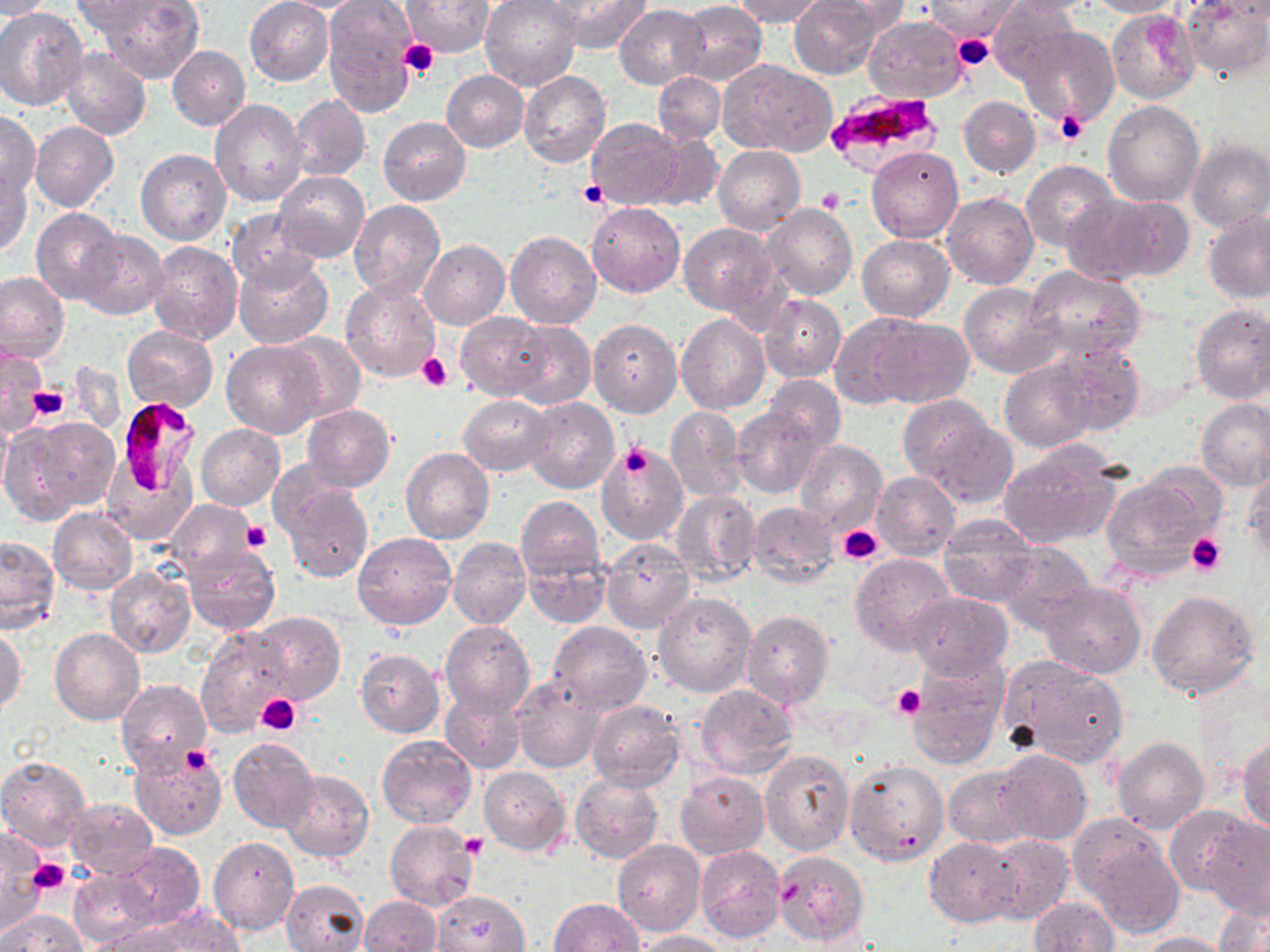
Summary:
  - Coordinate format: approximate bounding boxes as (x1, y1, x2, y2) in pixels
  - Uninfected red blood cell locations: (0, 0, 56, 19), (93, 0, 205, 84), (245, 0, 334, 85), (322, 0, 418, 118), (480, 0, 581, 92), (548, 0, 653, 52), (732, 0, 827, 26), (790, 0, 884, 79), (820, 0, 910, 39), (923, 0, 1022, 40), (987, 0, 1082, 89), (1002, 0, 1107, 15), (1087, 0, 1185, 18), (1181, 0, 1269, 81), (71, 1, 170, 37), (402, 1, 493, 57), (675, 2, 766, 84), (490, 5, 592, 165), (615, 5, 709, 89), (0, 8, 87, 111), (1107, 9, 1200, 104), (864, 15, 966, 104), (1021, 27, 1119, 128), (168, 45, 251, 132), (60, 47, 152, 140), (719, 60, 834, 156), (441, 70, 528, 152), (519, 70, 611, 168), (653, 71, 725, 144), (291, 95, 371, 181), (958, 96, 1039, 177), (210, 99, 307, 206), (1103, 99, 1204, 208), (0, 112, 40, 198), (379, 117, 471, 206), (584, 118, 682, 209), (30, 122, 119, 212), (651, 132, 724, 212), (1187, 140, 1270, 233), (713, 145, 805, 235), (867, 145, 963, 242), (136, 149, 232, 245), (1022, 160, 1120, 255), (0, 169, 32, 256), (274, 170, 369, 263), (942, 193, 1038, 290), (1063, 196, 1157, 282), (1105, 197, 1194, 281), (347, 200, 447, 302), (759, 202, 857, 300), (587, 203, 685, 297), (32, 207, 123, 304), (227, 209, 320, 291), (1203, 212, 1270, 304), (679, 223, 779, 319), (74, 231, 169, 320), (505, 231, 601, 328), (856, 235, 955, 322), (419, 239, 510, 330), (148, 241, 243, 346), (233, 255, 333, 349), (1024, 265, 1146, 363), (0, 272, 69, 365), (340, 278, 439, 380), (959, 282, 1061, 378), (759, 295, 846, 382), (1190, 304, 1270, 405), (455, 312, 553, 400), (676, 312, 770, 413), (830, 313, 932, 409), (866, 317, 974, 409), (588, 318, 682, 418), (506, 319, 595, 409), (123, 326, 217, 412), (276, 333, 366, 422), (1049, 340, 1144, 436), (221, 341, 326, 437), (0, 346, 46, 434), (1000, 359, 1098, 453), (761, 374, 846, 452), (458, 395, 552, 476), (521, 396, 620, 495), (1196, 399, 1270, 490), (302, 404, 395, 491), (665, 406, 747, 501), (734, 407, 825, 498), (0, 408, 12, 506), (913, 408, 1017, 506), (21, 416, 121, 514), (196, 423, 286, 511), (595, 440, 687, 542), (796, 440, 887, 536), (997, 443, 1123, 547), (401, 449, 494, 544), (103, 457, 195, 545), (1244, 466, 1270, 564), (871, 470, 960, 560), (1100, 474, 1218, 577), (280, 480, 373, 584), (671, 491, 760, 586), (516, 497, 605, 582), (165, 500, 256, 576), (746, 501, 839, 589), (48, 508, 138, 595), (938, 513, 1042, 606), (353, 531, 456, 629), (0, 536, 61, 633), (448, 536, 530, 630), (602, 539, 695, 633), (995, 543, 1094, 635), (182, 545, 280, 636), (523, 550, 613, 627), (849, 553, 954, 653), (104, 567, 193, 657), (1038, 580, 1145, 679), (1145, 589, 1261, 701), (653, 592, 756, 697), (905, 592, 1014, 680), (740, 610, 834, 709), (252, 611, 345, 703), (439, 621, 535, 720), (546, 621, 653, 713), (1, 626, 25, 716), (197, 626, 294, 739), (51, 629, 145, 725), (355, 649, 446, 738), (999, 656, 1129, 766), (907, 658, 1008, 768), (512, 674, 605, 773), (117, 680, 212, 776), (695, 684, 798, 778), (440, 692, 525, 774), (586, 699, 685, 790), (376, 733, 477, 827), (228, 736, 320, 834), (1238, 736, 1270, 834), (1113, 737, 1209, 834), (129, 746, 228, 839), (760, 748, 854, 854), (994, 751, 1093, 847), (0, 756, 91, 852), (845, 761, 948, 866), (479, 766, 570, 855), (943, 766, 1032, 848), (281, 769, 373, 862), (675, 771, 769, 859), (570, 773, 663, 864), (66, 799, 157, 879), (1165, 804, 1257, 896), (1197, 815, 1270, 917), (385, 819, 479, 911), (1074, 820, 1183, 933), (0, 829, 46, 934), (981, 832, 1074, 925), (925, 836, 1020, 927), (208, 837, 299, 935), (613, 840, 706, 937), (108, 842, 207, 932), (695, 845, 784, 942), (772, 850, 869, 946), (67, 867, 162, 945), (280, 880, 368, 951), (434, 891, 529, 951), (1029, 896, 1119, 952), (359, 897, 442, 951), (550, 898, 644, 952), (1214, 900, 1269, 952), (2, 908, 87, 952), (135, 908, 247, 952), (86, 925, 187, 952), (634, 929, 729, 951), (1134, 931, 1232, 951)
  - Plasmodium falciparum-infected red blood cell locations: (826, 88, 945, 174), (114, 396, 205, 498)
  - Platelet locations: (952, 32, 995, 72), (398, 40, 439, 79), (1055, 110, 1089, 146), (578, 181, 608, 209), (817, 187, 843, 213), (417, 352, 452, 392), (26, 385, 70, 422), (620, 442, 653, 480), (243, 520, 272, 552), (837, 524, 883, 565), (1184, 532, 1227, 576), (892, 684, 923, 720), (256, 693, 301, 734), (181, 746, 213, 773), (461, 832, 486, 857), (27, 858, 71, 897), (780, 883, 805, 904)
  - Slide-level diagnosis: Plasmodium falciparum
  - Field of view: single
  - Modality: light microscopy
  - Image size: 1270×952 pixels
  - Preparation: thin blood film
  - Magnification: 1000x
  - Stain: May-Grünwald-Giemsa